Outline each Plasmodium falciparum-infected red blood cell.
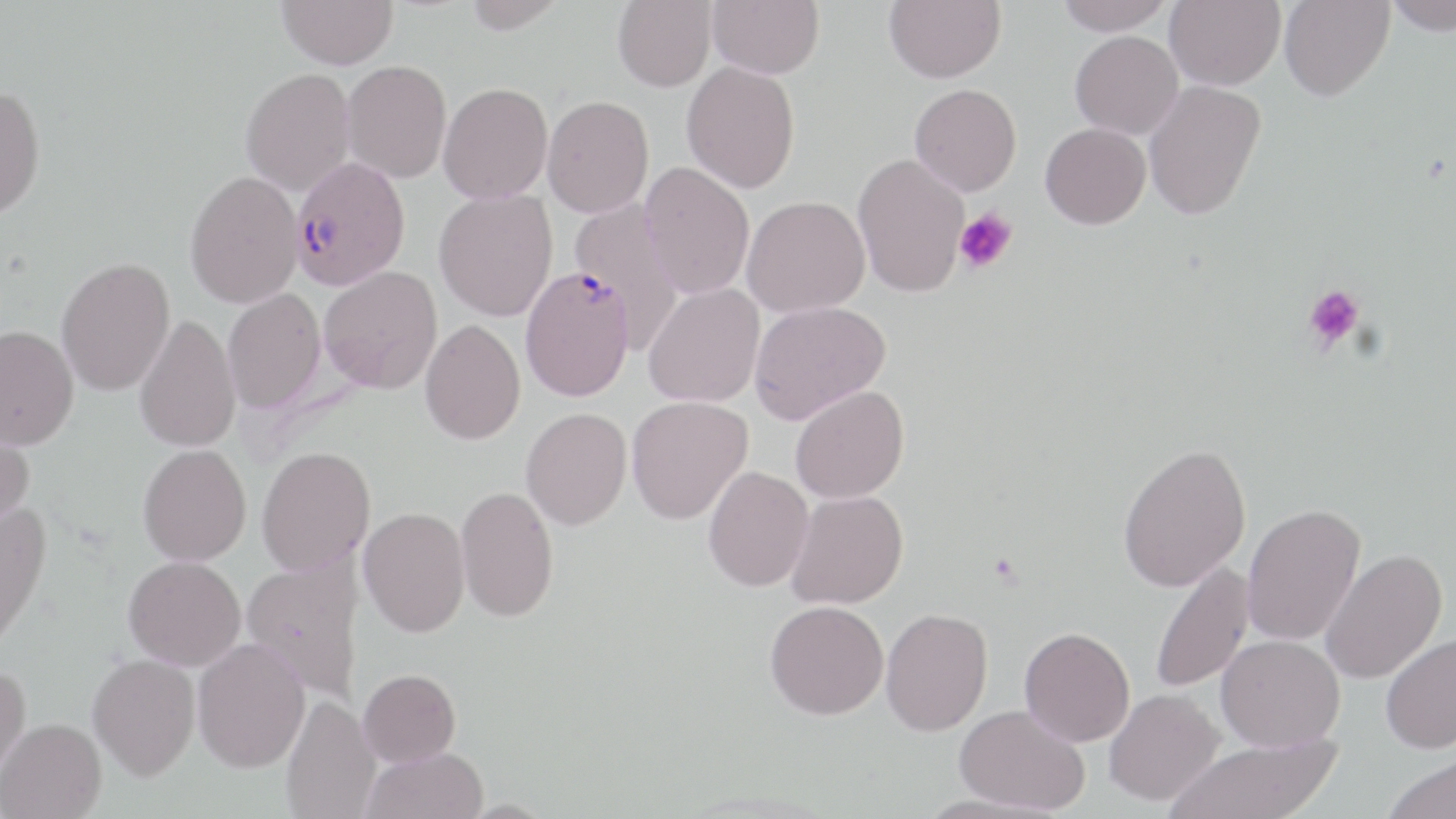

Approximate bounding boxes as (x1,y1)-(x2,y2) corner pairs in pixels.
Plasmodium falciparum-infected red blood cells: (289,156)-(411,290), (520,266)-(634,402).

Uninfected red blood cell locations: (276,0)-(398,70), (461,0)-(568,35), (613,0)-(716,92), (708,0)-(824,78), (884,0)-(1006,83), (1057,0)-(1175,34), (1165,0)-(1286,90), (1279,0)-(1394,101), (1386,0)-(1456,35), (1070,31)-(1184,139), (341,60)-(452,183), (681,62)-(800,193), (240,68)-(355,195), (1142,79)-(1266,220), (438,82)-(553,204), (909,83)-(1022,196), (0,84)-(46,220), (543,95)-(653,217), (1040,123)-(1151,229), (852,153)-(970,298), (639,162)-(755,299), (185,170)-(303,308), (434,189)-(558,321), (742,195)-(870,317), (569,198)-(685,353), (56,256)-(176,397), (319,266)-(442,394), (643,282)-(765,408), (223,288)-(326,414), (749,300)-(890,424), (134,314)-(241,453), (420,319)-(525,445), (0,323)-(79,450), (790,385)-(909,504), (626,396)-(753,524), (521,407)-(632,531), (0,421)-(35,534), (1117,443)-(1251,592), (138,444)-(251,566), (256,446)-(376,576), (703,466)-(814,592), (455,485)-(559,623), (786,490)-(908,609), (0,501)-(52,652), (1242,503)-(1366,647), (358,506)-(470,637), (1320,548)-(1448,684), (123,555)-(246,670), (240,556)-(366,702), (1149,560)-(1254,695), (765,600)-(889,720), (880,607)-(993,736), (1019,627)-(1135,747), (1380,632)-(1456,754), (1216,634)-(1344,752), (192,638)-(310,772), (87,653)-(200,780), (0,663)-(31,786), (358,669)-(461,767), (1103,688)-(1224,807), (281,693)-(381,819), (952,705)-(1090,814), (0,718)-(106,819), (1167,734)-(1340,819), (362,747)-(488,819), (1383,752)-(1456,819), (917,793)-(1068,819). Platelet locations: (953,208)-(1018,273), (1302,284)-(1366,353). Slide-level diagnosis: Plasmodium falciparum. Thin blood smear. Optical microscopy. May-Grünwald-Giemsa stain. Single field of view. Image is 1456×819 pixels. 1000x magnification.